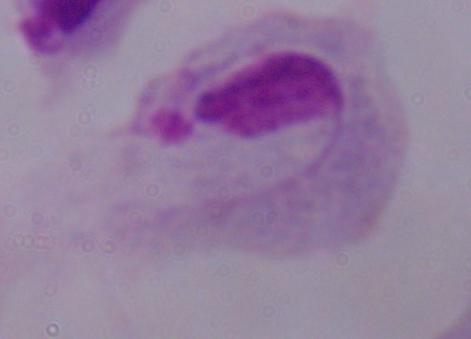

Summary:
  - Modality: photomicrograph
  - Magnification: 1000x
  - Identification: trichomonad